Describe the morphology of the red blood cells.
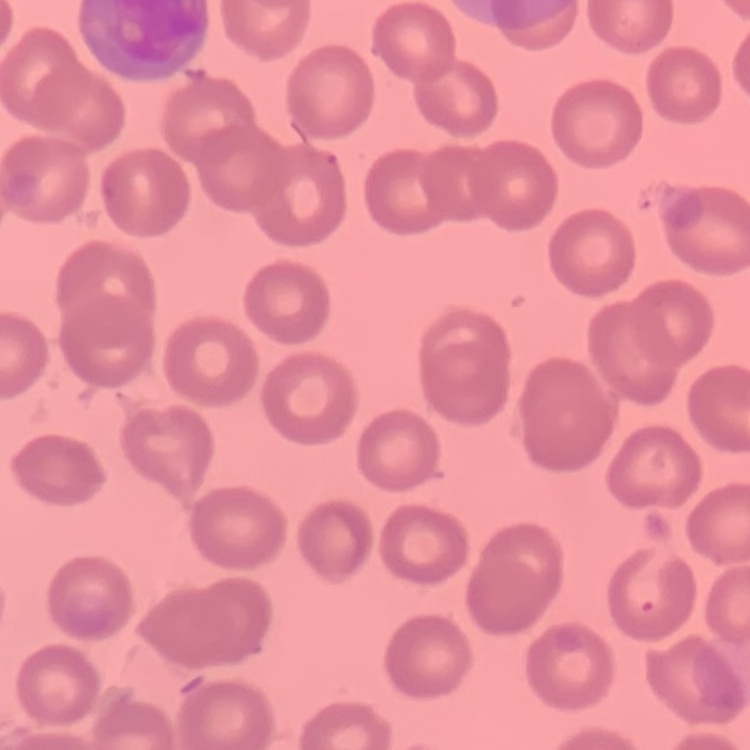
They show no rouleaux formation.

stain = Field's or Giemsa
preparation = thin peripheral smear
image type = square crop of a larger photomicrograph